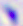
Summary:
  - Magnification: 400x
  - Modality: micrograph
  - Identification: Toxoplasma gondii